Identify the preparation type.
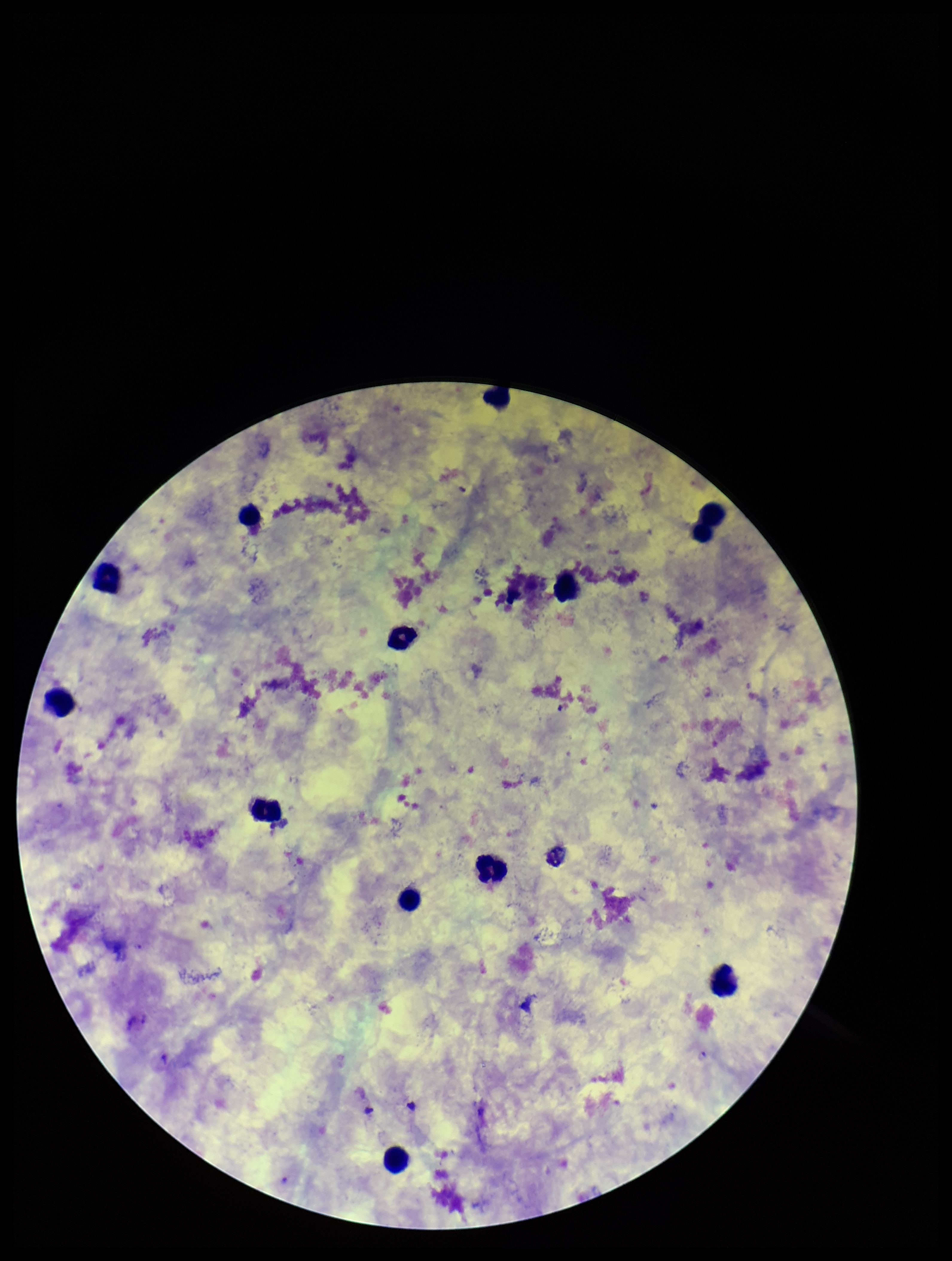

Thick.

parasite count = 0
patient malaria status = infected
stain = Giemsa
species reported for this patient = Plasmodium falciparum
Plasmodium parasites = none identified
leukocyte count = 12
capture = smartphone photograph through the microscope eyepiece
image size = 952×1261 pixels
field of view = one from this slide